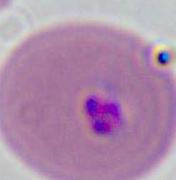
Summary:
  - Identification: Plasmodium
  - Magnification: 400x or 1000x
  - Modality: micrograph